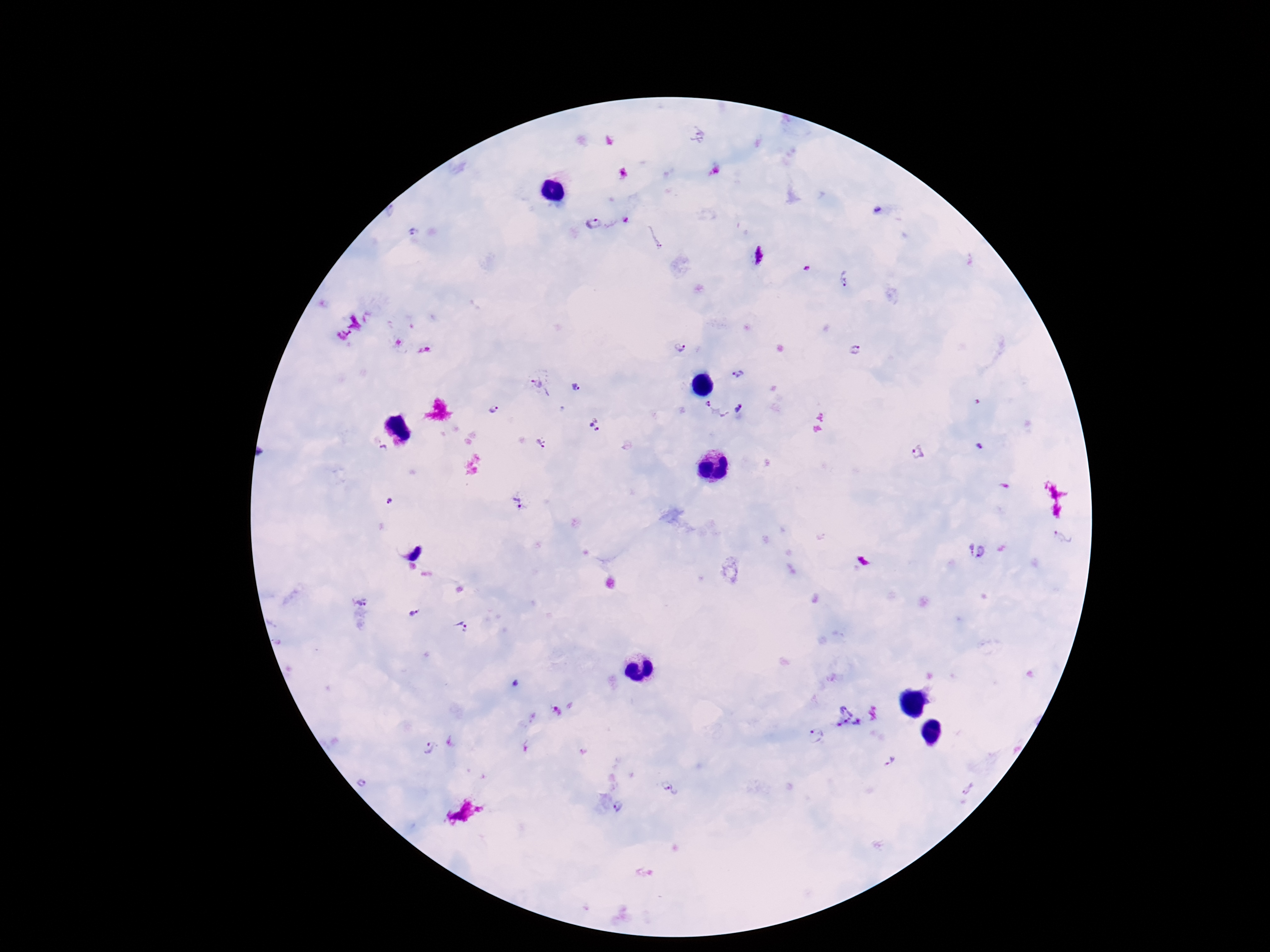

magnification: 100x
preparation: thick blood smear
capture: smartphone camera through the microscope eyepiece
image_size: 1270×952 pixels
plasmodium_parasite_locations: 'approximate centers as (x, y) in pixels: (594, 224), (844, 278), (678, 349), (856, 350), (739, 374), (539, 383), (575, 387), (708, 404), (739, 408), (494, 409), (596, 425), (540, 443), (979, 446), (384, 449), (920, 453), (520, 500), (389, 501), (1062, 537), (977, 550), (363, 598), (413, 613), (461, 627), (846, 716), (815, 735), (427, 747), (892, 759), (361, 782), (672, 789), (617, 807)'
field_of_view: single
patient_malaria_status: infected
stain: Giemsa